Classify this cell by malaria status.
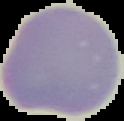
It is uninfected.

From a thin blood film. The area outside the segmented cell region is set to black. Image is 124×121 pixels.